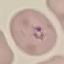

malaria status = parasitized
preparation = thin blood film
image type = cell patch, automatically extracted from a larger field of view and resized to 64 × 64 pixels
capture = smartphone camera at the microscope eyepiece
stain = Giemsa